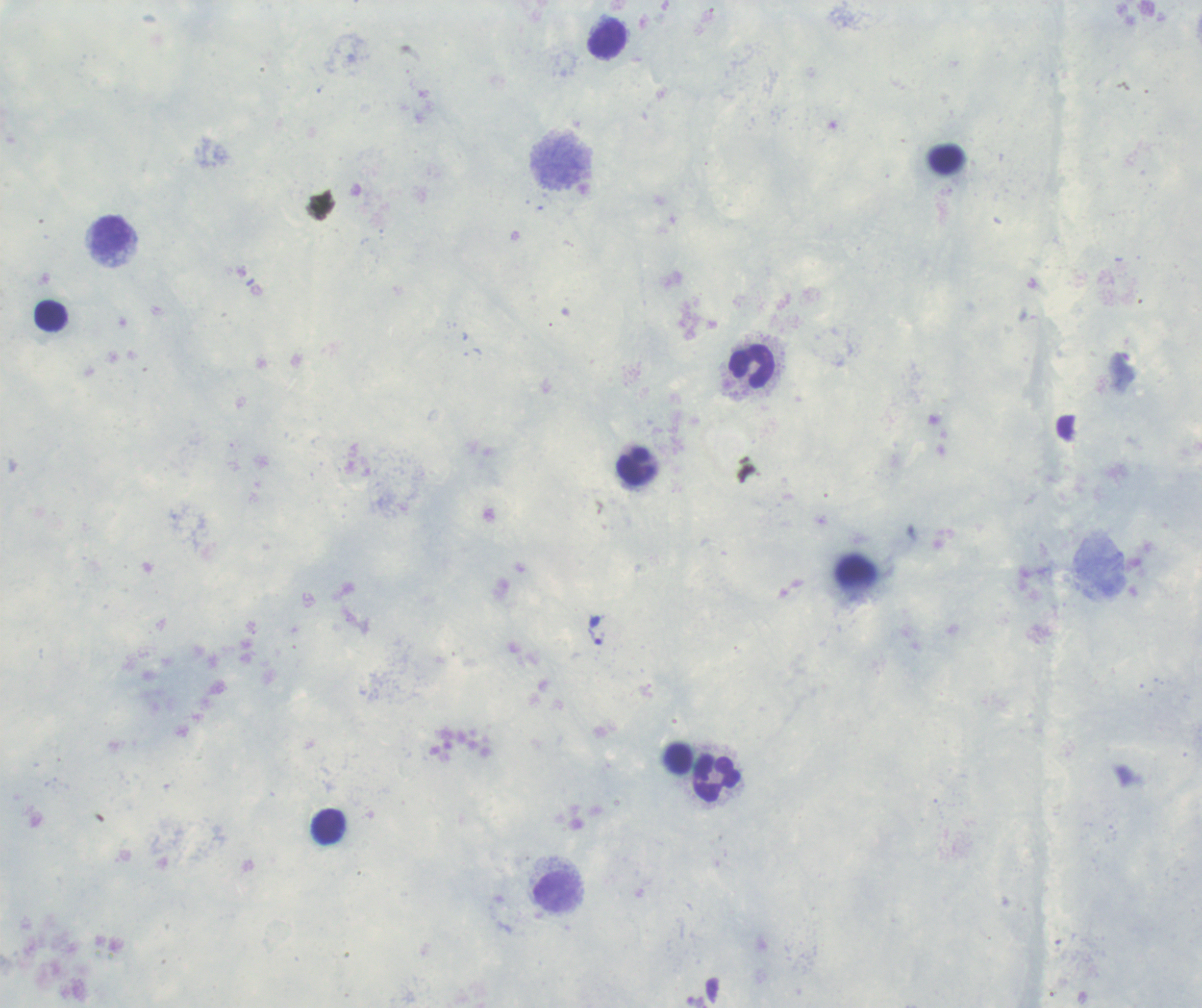
Approximate centers as (x, y) in pixels. Leukocyte locations: (608, 38), (559, 162), (113, 236), (52, 316), (753, 367), (636, 466), (717, 778), (329, 825), (557, 892). Trophozoite locations: (596, 636). Thick blood smear. Result: Plasmodium parasites identified. 100x magnification. Image is 1202×1008 pixels. Background quality: unsatisfactory. Previously used in an actual diagnosis. Coloration quality: good. Romanowsky stain. One field from this slide.